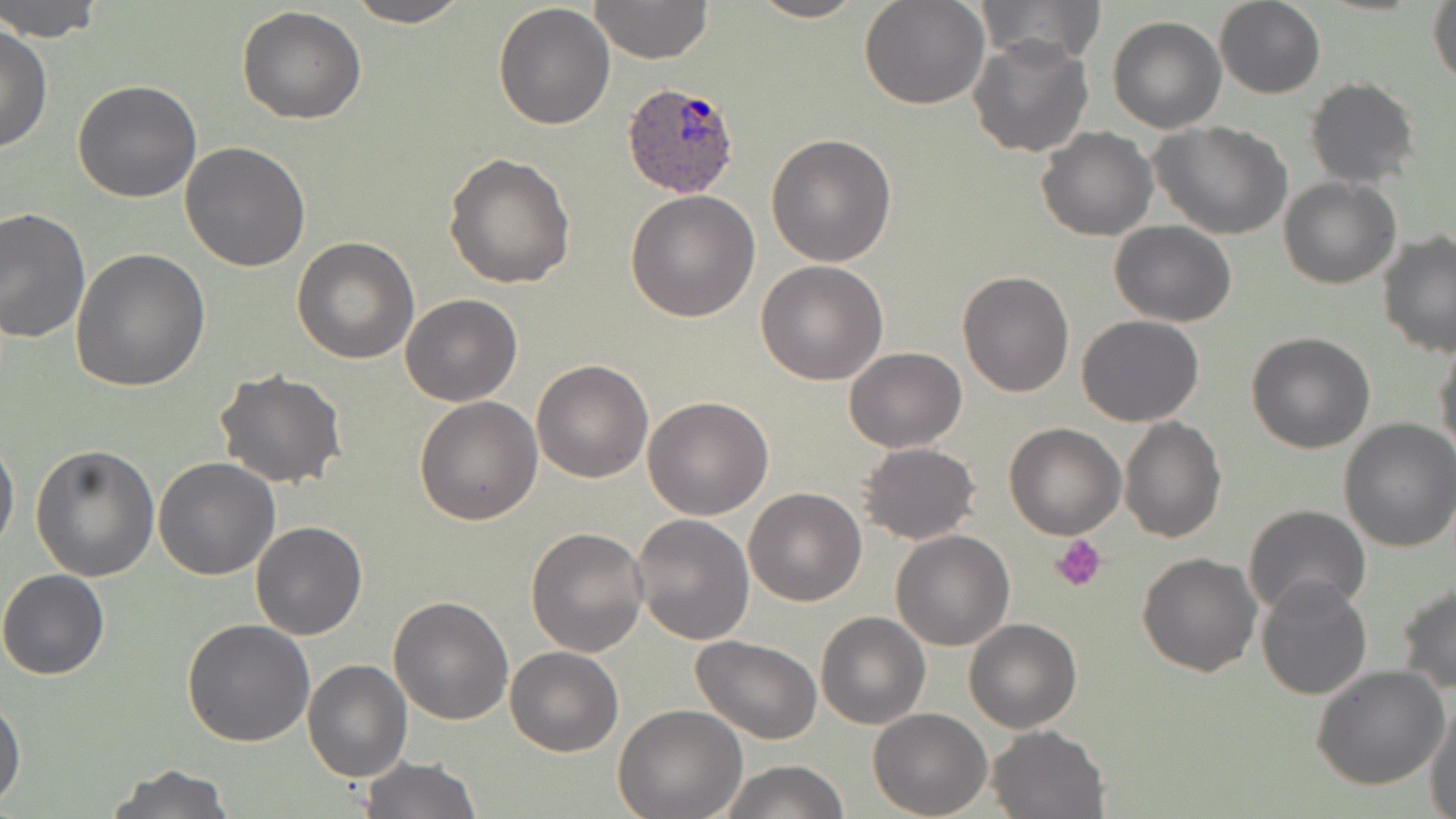

slide_level_diagnosis: Plasmodium ovale
preparation: thin blood smear
modality: light microscopy
magnification: 1000x
uninfected_red_blood_cell_locations: 'approximate bounding boxes as named x1/y1/x2/y2 corners in pixels: (x1=1, y1=0, x2=105, y2=42), (x1=345, y1=0, x2=472, y2=27), (x1=589, y1=0, x2=713, y2=65), (x1=747, y1=0, x2=867, y2=23), (x1=859, y1=0, x2=989, y2=109), (x1=979, y1=0, x2=1105, y2=65), (x1=1213, y1=0, x2=1326, y2=99), (x1=1428, y1=0, x2=1456, y2=90), (x1=493, y1=4, x2=616, y2=131), (x1=236, y1=6, x2=367, y2=125), (x1=1107, y1=17, x2=1227, y2=133), (x1=0, y1=25, x2=52, y2=155), (x1=967, y1=32, x2=1094, y2=157), (x1=1304, y1=76, x2=1421, y2=188), (x1=73, y1=80, x2=203, y2=202), (x1=1151, y1=122, x2=1294, y2=241), (x1=1036, y1=127, x2=1158, y2=241), (x1=765, y1=134, x2=897, y2=267), (x1=179, y1=140, x2=311, y2=270), (x1=444, y1=152, x2=577, y2=289), (x1=1280, y1=177, x2=1401, y2=289), (x1=626, y1=190, x2=760, y2=322), (x1=0, y1=207, x2=91, y2=343), (x1=1109, y1=220, x2=1237, y2=326), (x1=1378, y1=231, x2=1456, y2=358), (x1=292, y1=236, x2=420, y2=364), (x1=71, y1=249, x2=211, y2=395), (x1=755, y1=260, x2=889, y2=386), (x1=955, y1=270, x2=1074, y2=396), (x1=400, y1=293, x2=523, y2=406), (x1=1076, y1=314, x2=1203, y2=426), (x1=1245, y1=332, x2=1375, y2=454), (x1=1433, y1=340, x2=1456, y2=461), (x1=843, y1=346, x2=965, y2=452), (x1=531, y1=359, x2=653, y2=483), (x1=213, y1=368, x2=348, y2=490), (x1=414, y1=395, x2=543, y2=524), (x1=643, y1=396, x2=773, y2=520), (x1=1119, y1=415, x2=1227, y2=542), (x1=1337, y1=419, x2=1456, y2=554), (x1=1004, y1=421, x2=1127, y2=539), (x1=0, y1=435, x2=19, y2=556), (x1=856, y1=441, x2=981, y2=545), (x1=31, y1=442, x2=161, y2=581), (x1=152, y1=456, x2=281, y2=580), (x1=743, y1=488, x2=868, y2=606), (x1=1242, y1=504, x2=1371, y2=620), (x1=630, y1=514, x2=755, y2=646), (x1=250, y1=521, x2=368, y2=640), (x1=526, y1=527, x2=649, y2=657), (x1=891, y1=530, x2=1016, y2=650), (x1=1137, y1=551, x2=1262, y2=677), (x1=0, y1=569, x2=109, y2=680), (x1=1256, y1=575, x2=1373, y2=700), (x1=1397, y1=581, x2=1456, y2=693), (x1=387, y1=595, x2=513, y2=724), (x1=815, y1=611, x2=931, y2=729), (x1=964, y1=618, x2=1082, y2=734), (x1=182, y1=619, x2=315, y2=748), (x1=690, y1=635, x2=822, y2=744), (x1=505, y1=646, x2=622, y2=756), (x1=302, y1=659, x2=413, y2=783), (x1=1311, y1=666, x2=1451, y2=790), (x1=1, y1=696, x2=25, y2=807), (x1=1426, y1=699, x2=1456, y2=818), (x1=612, y1=703, x2=747, y2=819), (x1=868, y1=708, x2=993, y2=818), (x1=987, y1=724, x2=1109, y2=818), (x1=360, y1=756, x2=481, y2=819), (x1=720, y1=759, x2=849, y2=818), (x1=107, y1=763, x2=236, y2=818)'
plasmodium_ovale_infected_red_blood_cell_locations: 'approximate bounding boxes as named x1/y1/x2/y2 corners in pixels: (x1=620, y1=82, x2=742, y2=200)'
field_of_view: single
platelet_locations: 'approximate bounding boxes as named x1/y1/x2/y2 corners in pixels: (x1=1052, y1=535, x2=1105, y2=591)'
stain: May-Grünwald-Giemsa
image_size: 1456×819 pixels